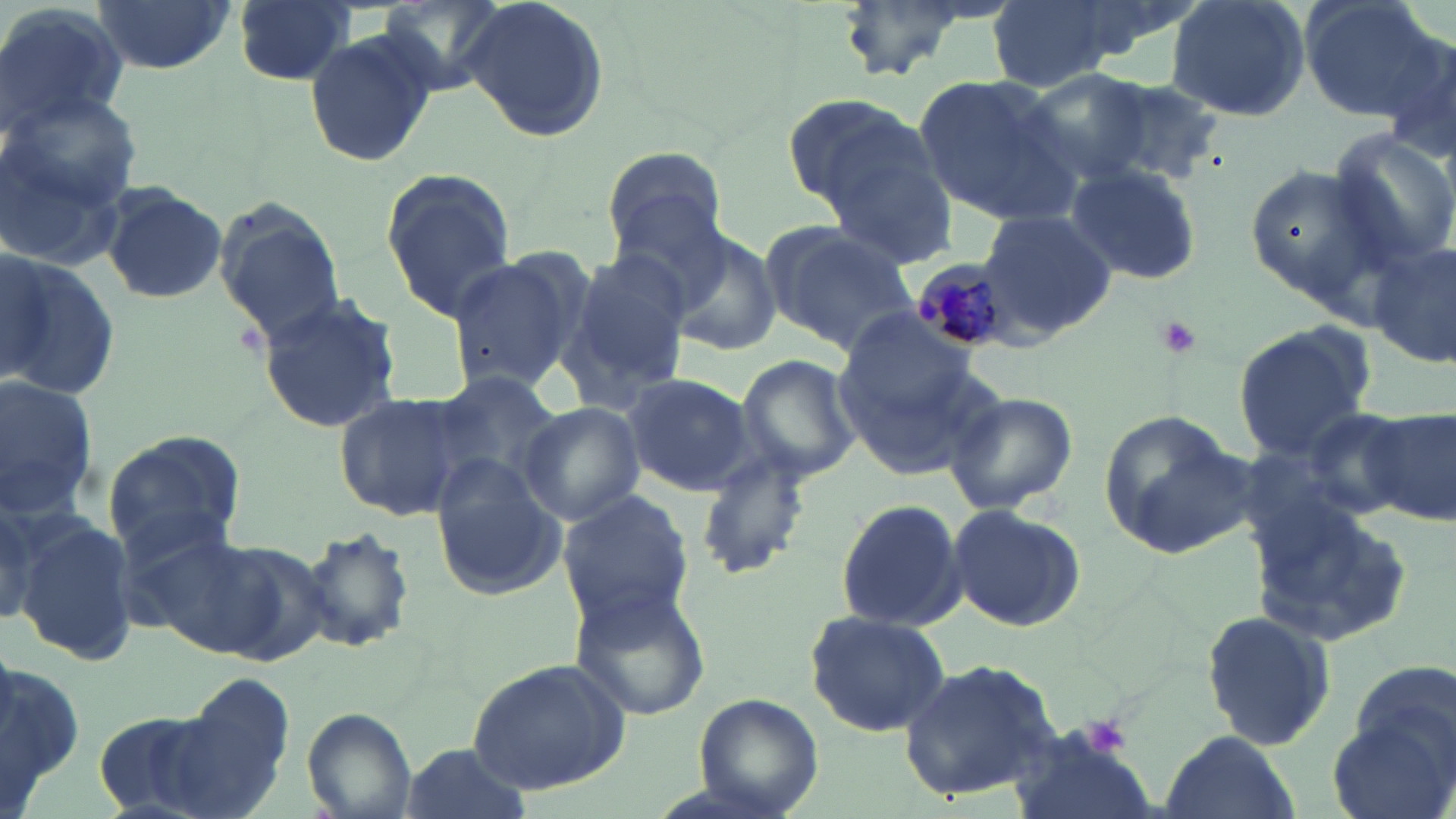
Approximate bounding boxes as (x1, y1, x2, y2) in pixels. Uninfected red blood cell locations: (230, 0, 359, 87), (375, 0, 510, 95), (459, 0, 610, 144), (832, 0, 979, 79), (986, 0, 1118, 92), (1055, 0, 1204, 74), (1166, 0, 1312, 123), (1298, 0, 1443, 121), (92, 1, 233, 75), (0, 3, 130, 141), (1376, 27, 1456, 161), (305, 29, 436, 171), (1021, 72, 1153, 183), (913, 76, 1077, 220), (1084, 76, 1229, 185), (3, 82, 143, 242), (780, 91, 925, 208), (1327, 130, 1456, 273), (818, 140, 959, 272), (601, 145, 731, 263), (1063, 162, 1203, 285), (1241, 162, 1393, 302), (378, 170, 516, 321), (625, 173, 765, 342), (99, 181, 226, 303), (214, 205, 343, 345), (978, 211, 1117, 333), (761, 222, 920, 353), (661, 228, 782, 357), (1371, 241, 1455, 370), (556, 249, 694, 412), (443, 251, 588, 395), (3, 257, 119, 403), (254, 293, 405, 434), (833, 322, 992, 478), (1232, 324, 1374, 457), (735, 353, 862, 486), (430, 369, 562, 491), (623, 372, 756, 496), (0, 376, 98, 521), (941, 389, 1079, 517), (332, 390, 476, 522), (518, 400, 645, 526), (1294, 402, 1426, 519), (1363, 403, 1455, 526), (1097, 411, 1255, 555), (101, 432, 247, 561), (691, 445, 814, 581), (430, 464, 566, 602), (555, 489, 695, 630), (835, 498, 967, 632), (0, 499, 43, 625), (1250, 500, 1417, 650), (948, 504, 1086, 631), (16, 519, 140, 668), (293, 525, 419, 657), (207, 542, 335, 664), (568, 585, 714, 722), (1201, 608, 1336, 753), (804, 611, 952, 737), (1, 648, 84, 819), (467, 658, 632, 795), (897, 658, 1065, 800), (1342, 658, 1456, 791), (157, 672, 298, 817), (691, 692, 822, 816), (301, 708, 416, 818), (1327, 711, 1454, 819), (1006, 722, 1160, 819), (1158, 732, 1300, 819), (400, 741, 531, 819). Platelet locations: (1154, 317, 1201, 360), (1080, 717, 1133, 757). Plasmodium malariae-infected red blood cell locations: (909, 261, 1009, 353). Slide-level diagnosis: Plasmodium malariae. Captured at 1000x magnification. Image is 1456×819 pixels. May-Grünwald-Giemsa-stained preparation. Single field of view. Thin blood film. Optical microscopy.